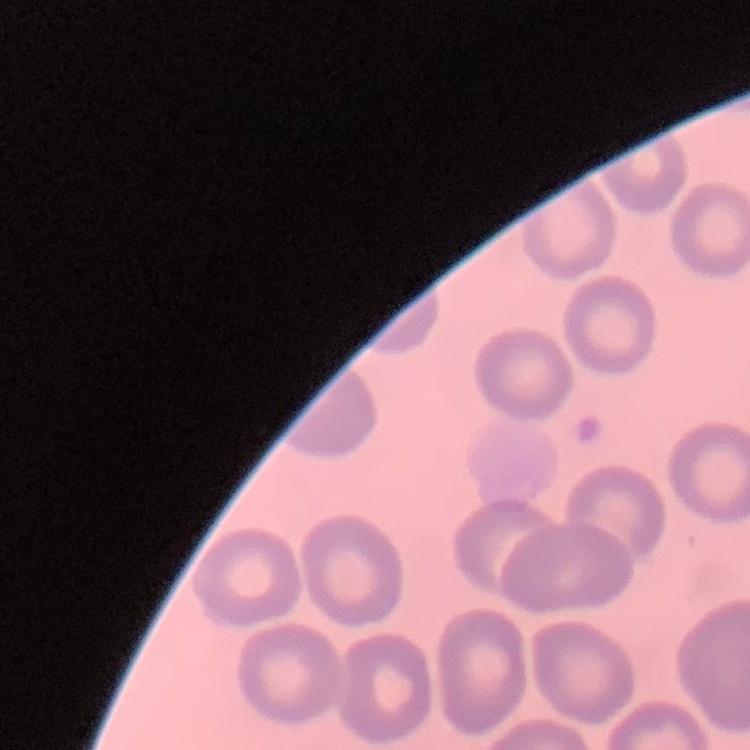

Summary:
  - Red blood cell morphology: no rouleaux formation
  - Preparation: thin peripheral smear
  - Image type: square crop of a larger photomicrograph
  - Stain: Field's or Giemsa